Name the cell type shown.
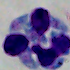

This is a leukocyte.

Summary:
  - Modality: photomicrograph
  - Magnification: 1000x